Give the extent of all uninfected red blood cells.
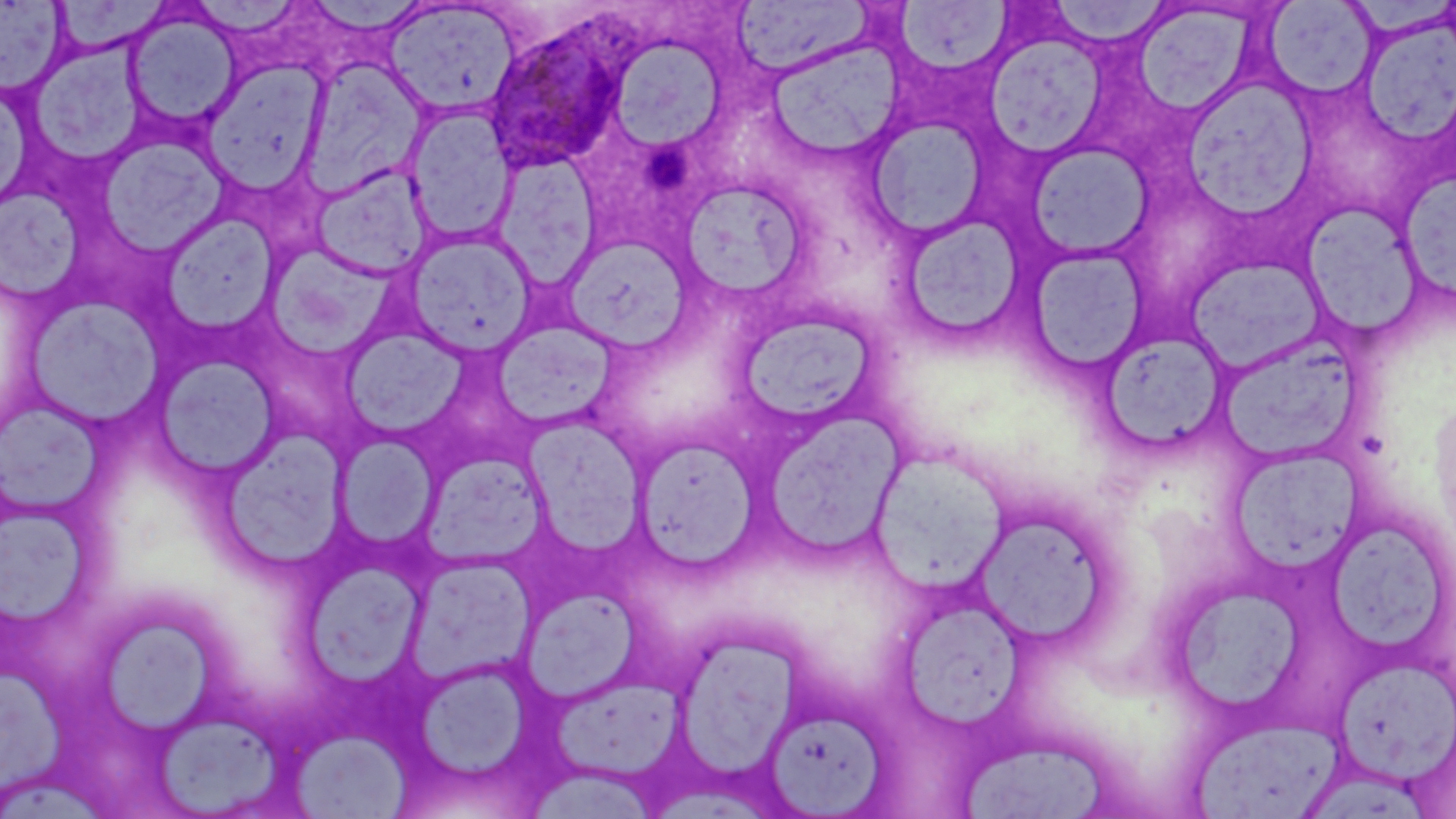
Approximate bounding boxes as (x1, y1, x2, y2) in pixels.
Uninfected red blood cells: (56, 0, 168, 54), (1043, 1, 1175, 49), (1, 2, 69, 94), (188, 2, 308, 39), (381, 2, 520, 118), (732, 2, 874, 80), (1265, 2, 1377, 99), (894, 3, 1014, 75), (1138, 10, 1256, 120), (124, 11, 241, 127), (1362, 17, 1456, 148), (985, 34, 1106, 156), (32, 38, 141, 170), (763, 38, 906, 163), (617, 39, 727, 151), (301, 56, 428, 198), (202, 62, 328, 192), (1178, 75, 1320, 216), (404, 104, 516, 246), (864, 116, 989, 241), (98, 136, 231, 256), (1023, 143, 1153, 261), (491, 152, 602, 290), (311, 164, 433, 280), (1401, 167, 1456, 305), (678, 177, 810, 302), (0, 188, 84, 297), (1300, 203, 1424, 337), (159, 212, 279, 334), (894, 213, 1028, 346), (403, 230, 538, 358), (559, 233, 694, 353), (263, 244, 396, 359), (1025, 246, 1149, 372), (1187, 256, 1327, 373), (25, 296, 163, 427), (731, 306, 886, 431), (491, 318, 618, 431), (342, 328, 466, 438), (1099, 329, 1229, 453), (1219, 335, 1361, 464), (151, 354, 281, 479), (0, 401, 103, 514), (750, 405, 909, 564), (524, 417, 646, 555), (218, 431, 349, 569), (333, 433, 442, 550), (632, 436, 760, 570), (1227, 445, 1364, 581), (863, 454, 1016, 603), (970, 508, 1119, 651), (0, 511, 92, 633), (1326, 522, 1443, 656), (407, 554, 535, 683), (303, 561, 424, 684), (1166, 583, 1304, 717), (521, 589, 642, 704), (904, 600, 1031, 738), (103, 616, 213, 734), (676, 636, 814, 782), (1333, 655, 1456, 783), (417, 663, 530, 785), (0, 667, 72, 801), (548, 675, 684, 780), (762, 705, 889, 817), (155, 713, 292, 818), (1193, 717, 1342, 818), (293, 731, 413, 817), (956, 736, 1114, 816), (524, 766, 665, 819).

Plasmodium ovale-infected red blood cell locations = approximate bounding boxes as (x1, y1, x2, y2) in pixels: (482, 19, 631, 172)
slide-level diagnosis = Plasmodium ovale
stain = May-Grünwald-Giemsa
preparation = thin blood film
magnification = 1000x
modality = optical microscopy
image size = 1456×819 pixels
field of view = one of a larger specimen